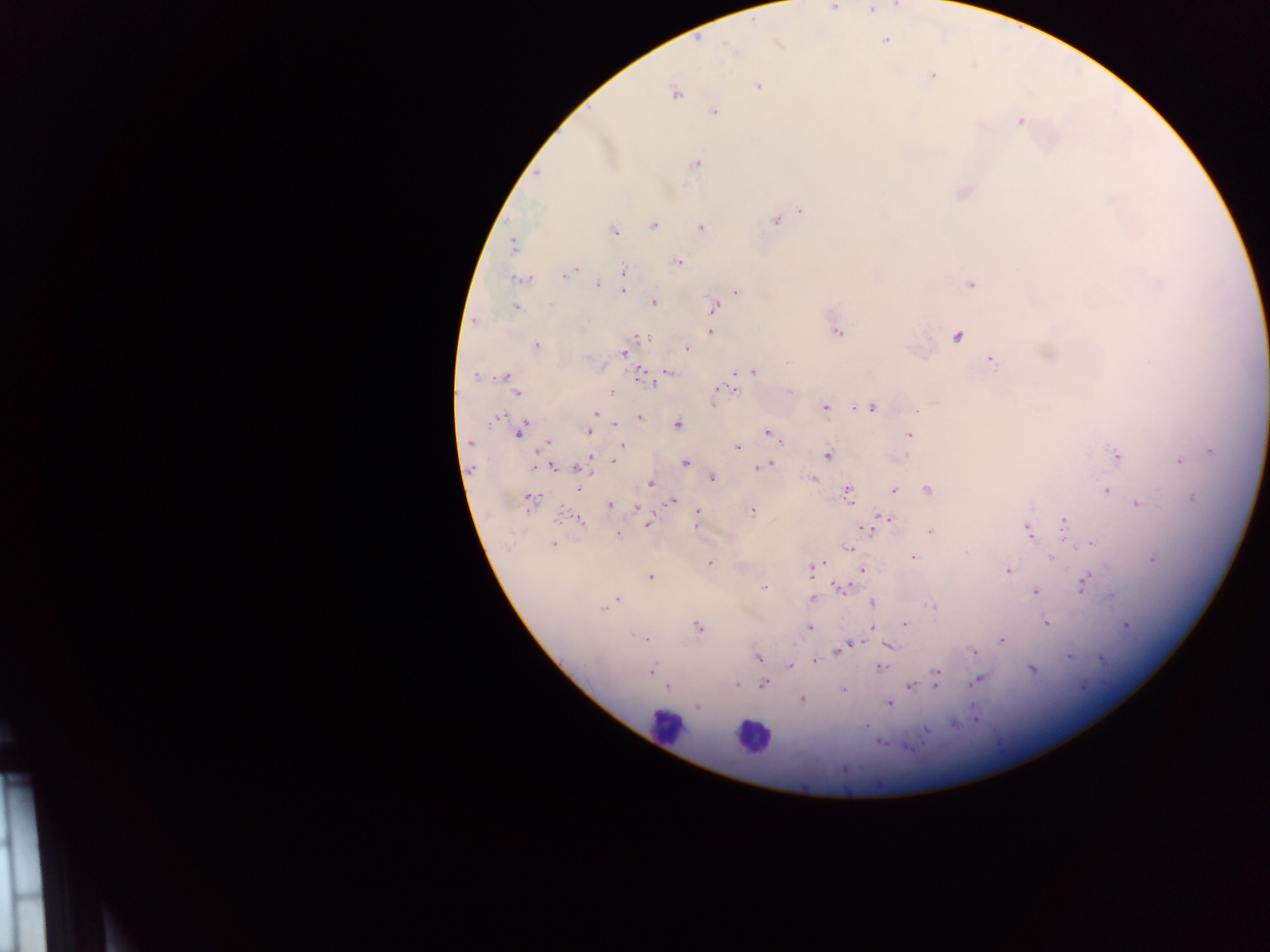

Approximate centers as {x, y} in pixels.
Summary:
  - Plasmodium parasite locations: {834, 6}, {870, 10}, {885, 40}, {778, 44}, {932, 75}, {758, 86}, {675, 93}, {714, 112}, {1021, 121}, {696, 164}, {537, 173}, {802, 210}, {775, 221}, {654, 225}, {701, 227}, {614, 230}, {513, 245}, {679, 262}, {576, 270}, {624, 270}, {565, 275}, {522, 279}, {624, 281}, {971, 284}, {597, 285}, {623, 290}, {737, 291}, {654, 302}, {550, 305}, {516, 306}, {714, 307}, {474, 321}, {710, 332}, {838, 333}, {957, 336}, {642, 338}, {536, 346}, {687, 348}, {623, 353}, {991, 359}, {752, 371}, {668, 372}, {476, 375}, {640, 375}, {504, 376}, {645, 380}, {652, 383}, {729, 389}, {717, 391}, {611, 392}, {518, 394}, {825, 407}, {852, 407}, {871, 407}, {917, 411}, {596, 414}, {499, 417}, {640, 417}, {614, 424}, {678, 424}, {591, 425}, {519, 431}, {588, 432}, {767, 432}, {909, 435}, {781, 441}, {469, 443}, {547, 443}, {622, 445}, {737, 447}, {1212, 451}, {828, 455}, {1117, 456}, {614, 460}, {1179, 461}, {686, 462}, {769, 465}, {535, 466}, {552, 467}, {576, 467}, {761, 467}, {712, 477}, {813, 478}, {651, 484}, {580, 489}, {894, 490}, {927, 490}, {1106, 491}, {847, 492}, {531, 499}, {1192, 499}, {672, 500}, {1138, 503}, {610, 505}, {637, 508}, {752, 511}, {698, 513}, {885, 518}, {579, 520}, {1064, 522}, {875, 523}, {648, 524}, {696, 524}, {866, 529}, {1027, 530}, {930, 532}, {618, 533}, {1089, 544}, {553, 545}, {849, 548}, {913, 557}, {1053, 558}, {1153, 560}, {709, 563}, {822, 563}, {813, 566}, {862, 570}, {1007, 571}, {651, 576}, {1084, 582}, {763, 587}, {840, 587}, {1035, 591}, {813, 598}, {617, 599}, {873, 603}, {933, 606}, {602, 609}, {1047, 623}, {904, 625}, {1126, 626}, {697, 627}, {810, 627}, {873, 628}, {635, 636}, {643, 637}, {1001, 641}, {855, 643}, {845, 647}, {888, 647}, {839, 651}, {973, 651}, {1069, 657}, {758, 658}, {1101, 659}, {814, 660}, {790, 665}, {880, 668}, {1032, 669}, {651, 670}, {937, 673}, {978, 680}, {736, 684}, {764, 685}, {935, 685}, {911, 686}, {667, 688}, {842, 689}, {802, 699}, {889, 704}, {697, 706}, {954, 725}, {926, 730}
  - Leukocyte locations: {665, 725}, {751, 737}
  - Field of view: single
  - Country: Ghana
  - Image size: 1270×952 pixels
  - Preparation: thick blood smear
  - Capture: mobile-phone photograph through a microscope